State which parasite is depicted.
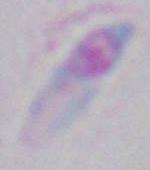

This is Toxoplasma gondii.

Micrograph. 1000x magnification.